Report the malaria status of this cell.
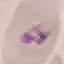

It is parasitized.

{
  "stain": "Giemsa",
  "image_type": "automatically extracted cell patch, resized to 64 × 64 pixels",
  "capture": "smartphone camera at the microscope eyepiece",
  "preparation": "thin blood film"
}